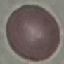
Summary:
  - Malaria status: uninfected
  - Capture: smartphone camera at the microscope eyepiece
  - Stain: Giemsa
  - Preparation: thin blood smear
  - Image type: automatically extracted cell patch, resized to 64 × 64 pixels